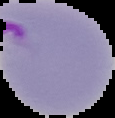

Image is 115×118 pixels. Cell region segmented out of the field of view; the surrounding area is masked to black. From a thin blood film. Result: Plasmodium parasites identified.